Classify this cell by malaria status.
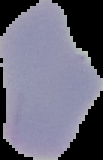

Uninfected.

Segmented cell region on a black background. Image is 103×160 pixels. From a thin blood smear.